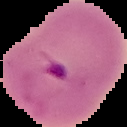
Summary:
  - Image type: cell region segmented out of the field of view; surrounding area masked to black
  - Image size: 127×127 pixels
  - Preparation: thin blood film
  - Result: Plasmodium parasites detected